Assess this cell for malaria.
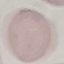

It is uninfected.

Summary:
  - Preparation: thin blood film
  - Stain: Giemsa
  - Capture: smartphone through the microscope eyepiece
  - Image type: automatically extracted cell patch, resized to 64 × 64 pixels